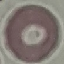

Summary:
  - Malaria status: uninfected
  - Capture: smartphone through the microscope eyepiece
  - Image type: cell patch, automatically extracted from a larger field of view and resized to 64 × 64 pixels
  - Stain: Giemsa
  - Preparation: thin blood smear